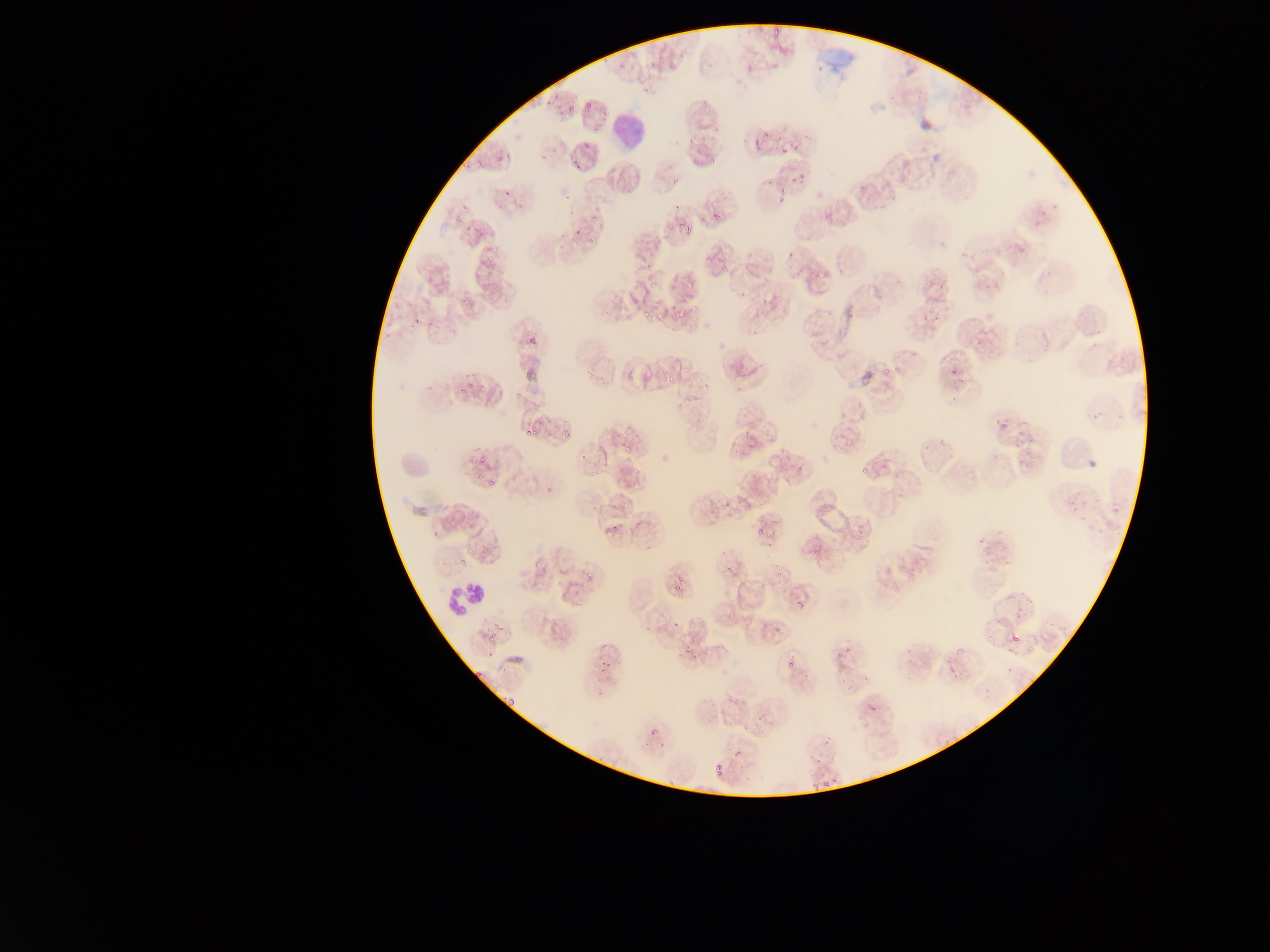

Approximate bounding boxes as [left, top, right, bottom] in pixels.
Summary:
  - Leukocyte locations: [612, 111, 648, 149], [440, 578, 487, 618]
  - Plasmodium parasite locations: [754, 139, 762, 147], [497, 154, 507, 164], [778, 196, 786, 205], [670, 221, 696, 238], [573, 228, 582, 236], [716, 261, 732, 275], [686, 278, 700, 292], [693, 303, 699, 312], [637, 308, 659, 322], [673, 311, 686, 319], [528, 336, 537, 345], [974, 339, 982, 346], [952, 367, 960, 376], [621, 370, 634, 382], [667, 371, 678, 382], [456, 377, 476, 396], [523, 425, 537, 443], [475, 455, 487, 466], [860, 466, 868, 473], [472, 472, 482, 482], [487, 478, 495, 486], [731, 495, 768, 513], [606, 517, 628, 536], [756, 528, 770, 534], [458, 556, 467, 566], [584, 568, 597, 583], [672, 581, 681, 592], [791, 603, 804, 613], [487, 625, 501, 645], [1011, 635, 1020, 644], [602, 641, 610, 650], [681, 645, 697, 659], [787, 658, 794, 667], [601, 660, 609, 669], [504, 697, 513, 706], [650, 728, 658, 737], [734, 748, 743, 756], [713, 763, 723, 776] | approximate [x, y] pixel centers of objects too small to bound: [717, 217], [790, 255], [416, 322], [838, 655], [873, 708]
  - Country: Ghana
  - Image size: 1270×952 pixels
  - Capture: mobile-phone photograph through a microscope
  - Field of view: single
  - Preparation: thin blood smear